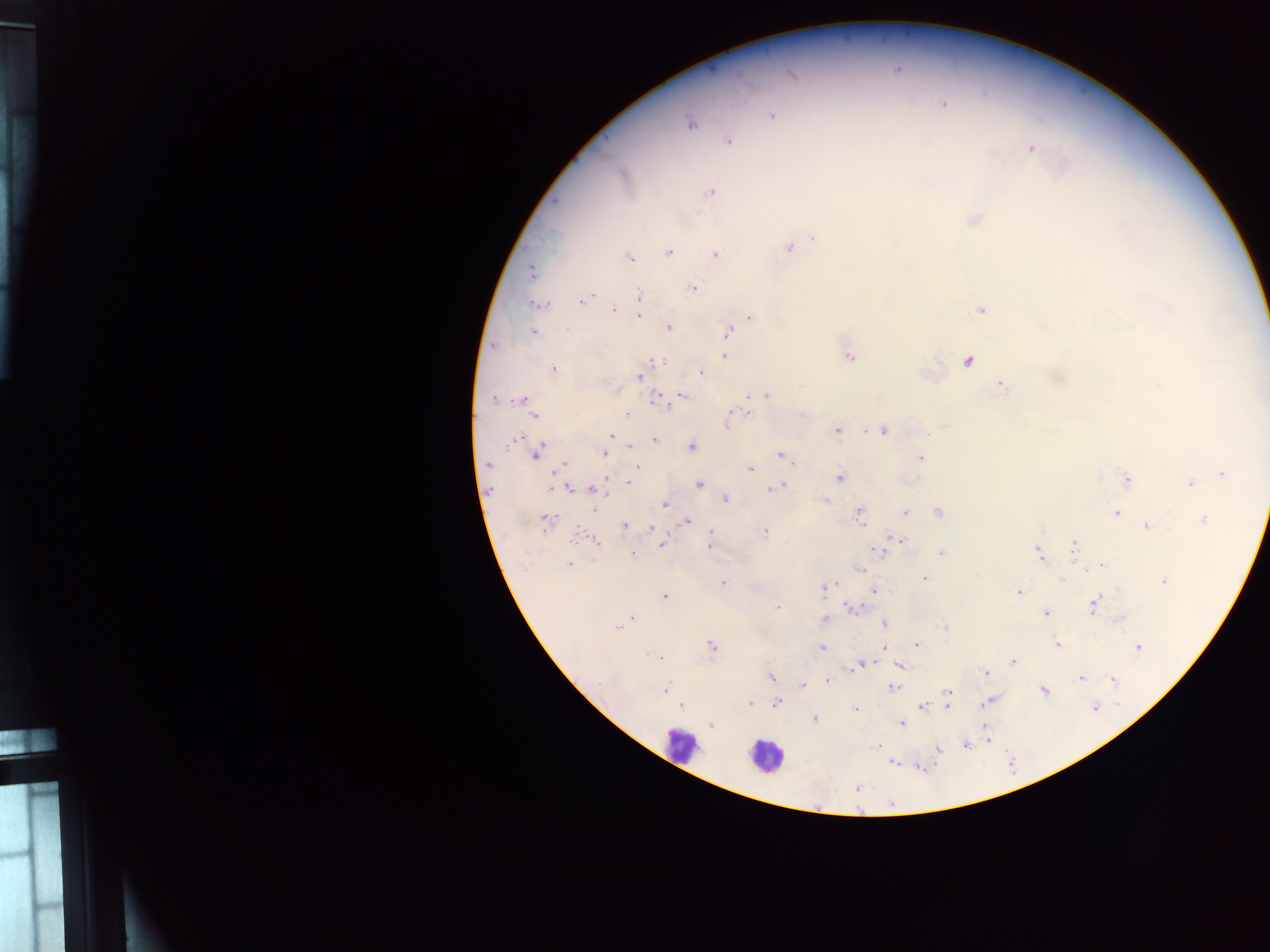
Approximate centers as x y in pixels. Leukocyte locations: 680 744; 765 756. Malaria parasite locations: 943 103; 771 115; 690 124; 729 142; 1031 149; 712 192; 974 220; 814 239; 788 247; 668 253; 715 255; 629 257; 532 271; 692 288; 639 295; 589 296; 582 301; 534 305; 544 305; 613 310; 981 310; 639 315; 750 317; 668 326; 567 329; 533 332; 728 332; 725 355; 848 357; 967 361; 659 362; 553 370; 701 373; 639 376; 1002 385; 682 395; 765 395; 494 399; 522 399; 655 399; 626 413; 748 413; 534 415; 730 418; 727 424; 838 430; 884 430; 610 436; 514 438; 654 440; 630 446; 692 446; 538 453; 603 454; 780 454; 920 458; 487 464; 565 464; 637 466; 749 468; 1223 473; 840 478; 1126 479; 630 482; 698 484; 1190 484; 780 486; 567 489; 772 489; 595 490; 726 499; 826 501; 665 505; 594 509; 939 512; 905 513; 1117 513; 860 514; 1203 519; 547 520; 687 521; 625 525; 1147 525; 652 528; 710 532; 764 532; 898 539; 597 541; 662 544; 708 545; 1073 546; 876 550; 1038 551; 941 553; 632 554; 569 563; 1102 565; 860 569; 924 578; 1062 579; 1164 581; 723 582; 825 589; 875 591; 1018 592; 665 597; 1093 605; 776 608; 852 609; 1047 613; 631 618; 824 619; 884 624; 617 628; 1057 643; 917 644; 711 645; 1139 646; 822 648; 884 648; 647 655; 659 657; 1013 661; 862 664; 902 666; 985 672; 771 677; 1081 678; 1113 679; 828 681; 803 684; 894 688; 665 690; 1044 691; 950 692; 948 696; 987 702; 750 703; 777 703; 682 705; 923 706; 947 707; 1095 707; 855 709; 814 719; 901 722; 712 725; 984 729; 878 745; 966 745; 939 749; 892 763. One field of view. Image is 1270×952 pixels. Thick blood smear. Collected in Ghana. Mobile-phone photograph taken through the microscope.